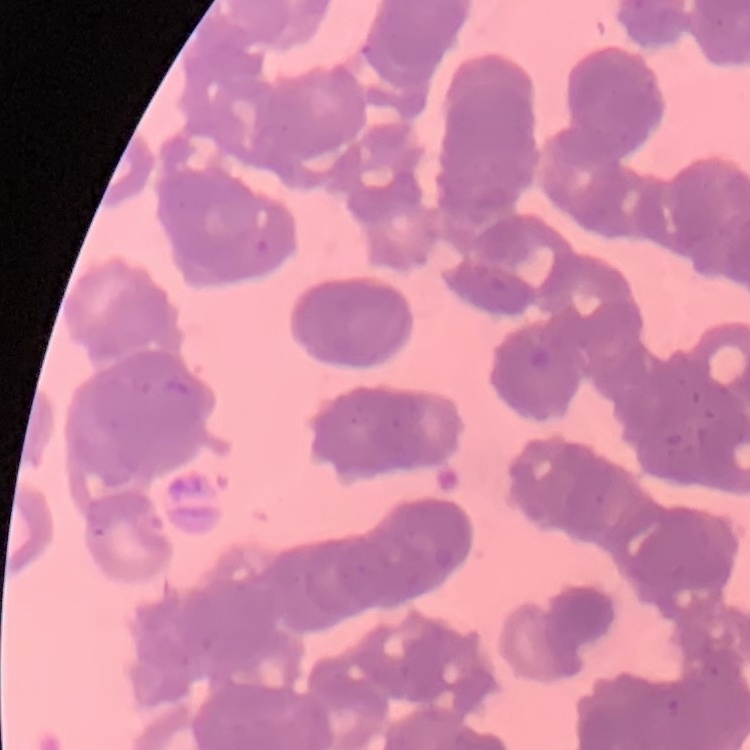
The erythrocytes show rouleaux formation. Thin blood smear. Stained with either Field's or Giemsa. One tile cut from a larger photomicrograph.